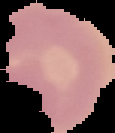
Image is 115×133 pixels. From a thin blood smear. Cell region segmented out of the field of view; the surrounding area is masked to black. Result: no malaria parasites seen.